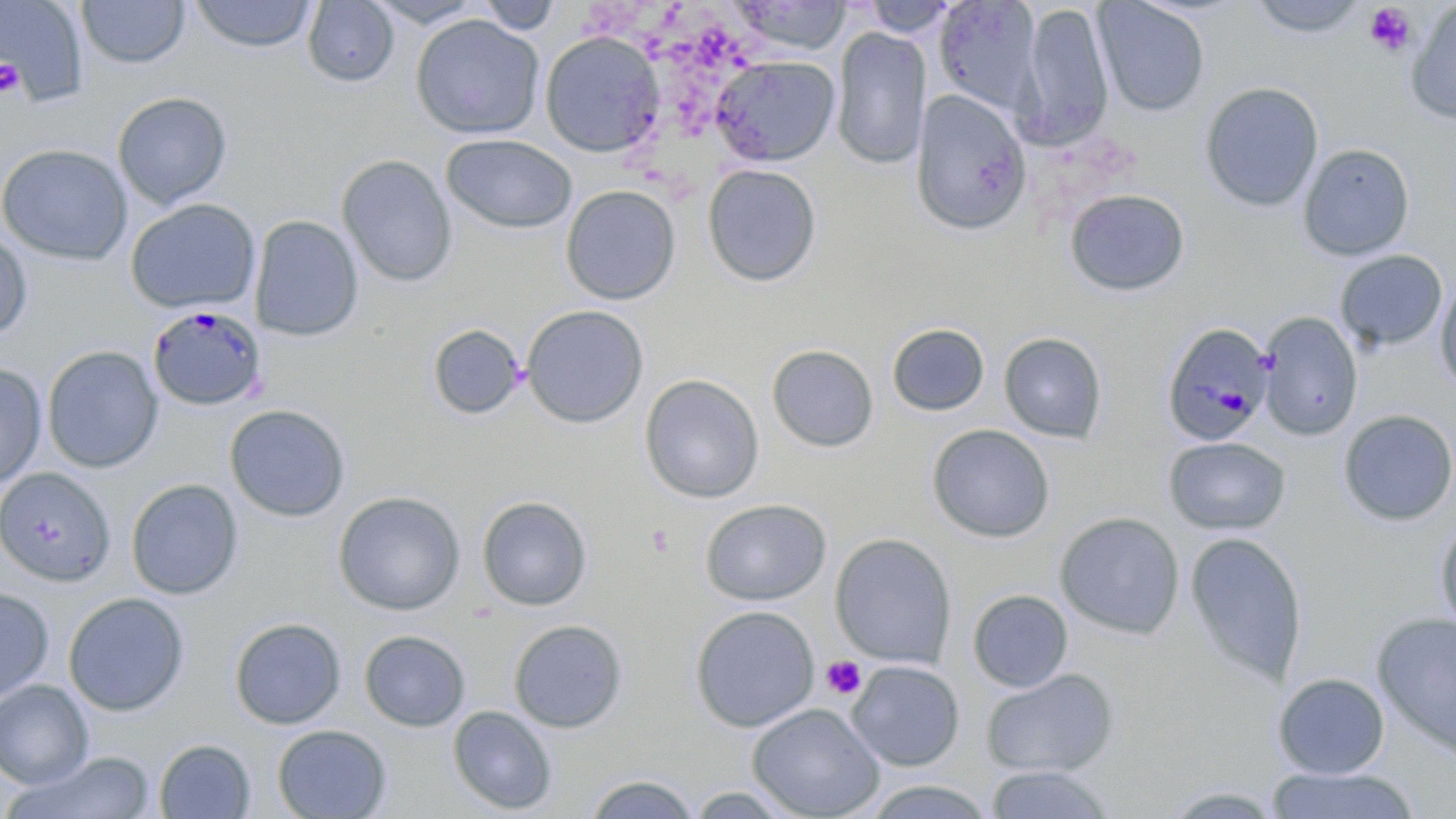 Approximate bounding boxes as (x1,y1)-(x2,y2) corner pairs in pixels. Platelet locations: (1364,2)-(1418,56), (0,58)-(24,97), (821,655)-(866,700). Plasmodium malariae-infected red blood cell locations: (147,305)-(267,412), (1161,321)-(1275,447). Uninfected red blood cell locations: (1,0)-(89,104), (366,0)-(488,28), (728,0)-(851,55), (1093,0)-(1211,117), (1247,0)-(1372,38), (77,1)-(189,69), (189,1)-(318,53), (302,1)-(399,88), (476,1)-(564,35), (859,1)-(963,38), (933,1)-(1042,116), (1405,2)-(1456,126), (1019,3)-(1114,147), (410,14)-(545,139), (831,26)-(931,171), (539,31)-(666,158), (711,54)-(840,166), (1199,81)-(1324,212), (910,90)-(1032,237), (112,91)-(232,210), (441,134)-(578,235), (1298,143)-(1415,262), (0,144)-(133,266), (337,154)-(458,287), (702,163)-(822,287), (560,184)-(681,305), (1064,188)-(1190,297), (125,198)-(261,314), (249,214)-(364,342), (0,226)-(33,340), (1335,250)-(1448,351), (1435,277)-(1456,394), (521,305)-(650,429), (1257,312)-(1363,441), (887,323)-(989,417), (426,324)-(526,420), (999,332)-(1108,443), (766,344)-(879,453), (42,346)-(163,473), (0,362)-(47,490), (640,374)-(764,503), (224,404)-(350,522), (1338,409)-(1456,526), (927,424)-(1055,543), (1163,436)-(1291,536), (0,467)-(116,586), (125,478)-(244,600), (333,491)-(466,616), (476,495)-(592,611), (700,498)-(832,606), (1054,511)-(1185,639), (1433,520)-(1456,635), (1184,531)-(1308,688), (829,532)-(957,669), (0,587)-(54,703), (967,589)-(1074,692), (63,592)-(189,717), (689,605)-(820,732), (1372,611)-(1456,760), (229,617)-(347,729), (508,619)-(628,733), (359,629)-(471,732), (847,660)-(965,772), (981,668)-(1120,777), (1273,672)-(1391,778), (0,680)-(93,790), (747,702)-(885,818), (447,705)-(558,815), (272,724)-(392,818), (154,738)-(255,818), (7,751)-(156,819), (983,764)-(1117,819), (1265,765)-(1420,818), (583,773)-(699,818), (859,779)-(997,819), (680,784)-(802,817). Slide-level diagnosis: Plasmodium malariae. One field of a larger specimen. Light microscopy. May-Grünwald-Giemsa-stained preparation. Image is 1456×819 pixels. Thin blood film. 1000x magnification.